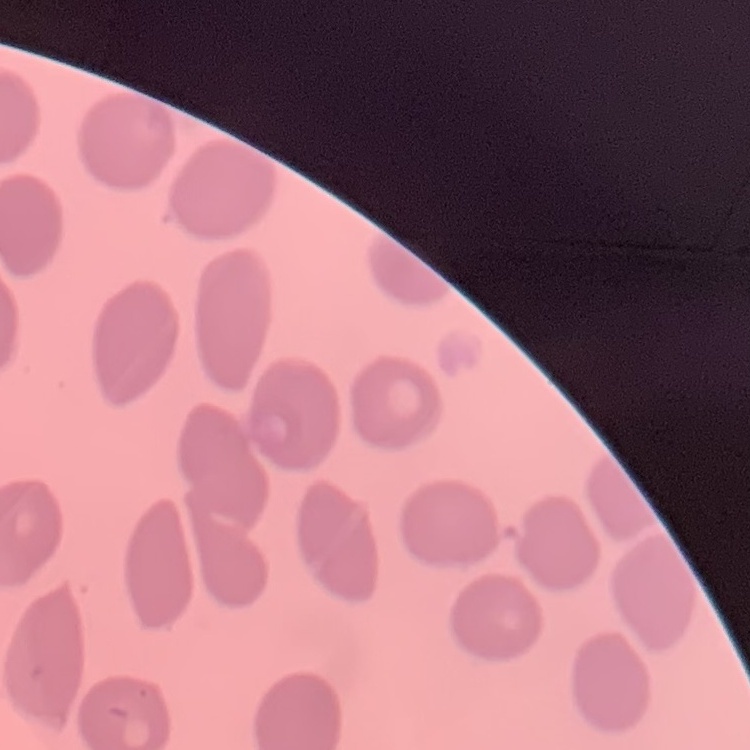
erythrocyte morphology = no rouleaux formation
stain = Field's or Giemsa
image type = square crop of a larger photomicrograph
preparation = thin blood film